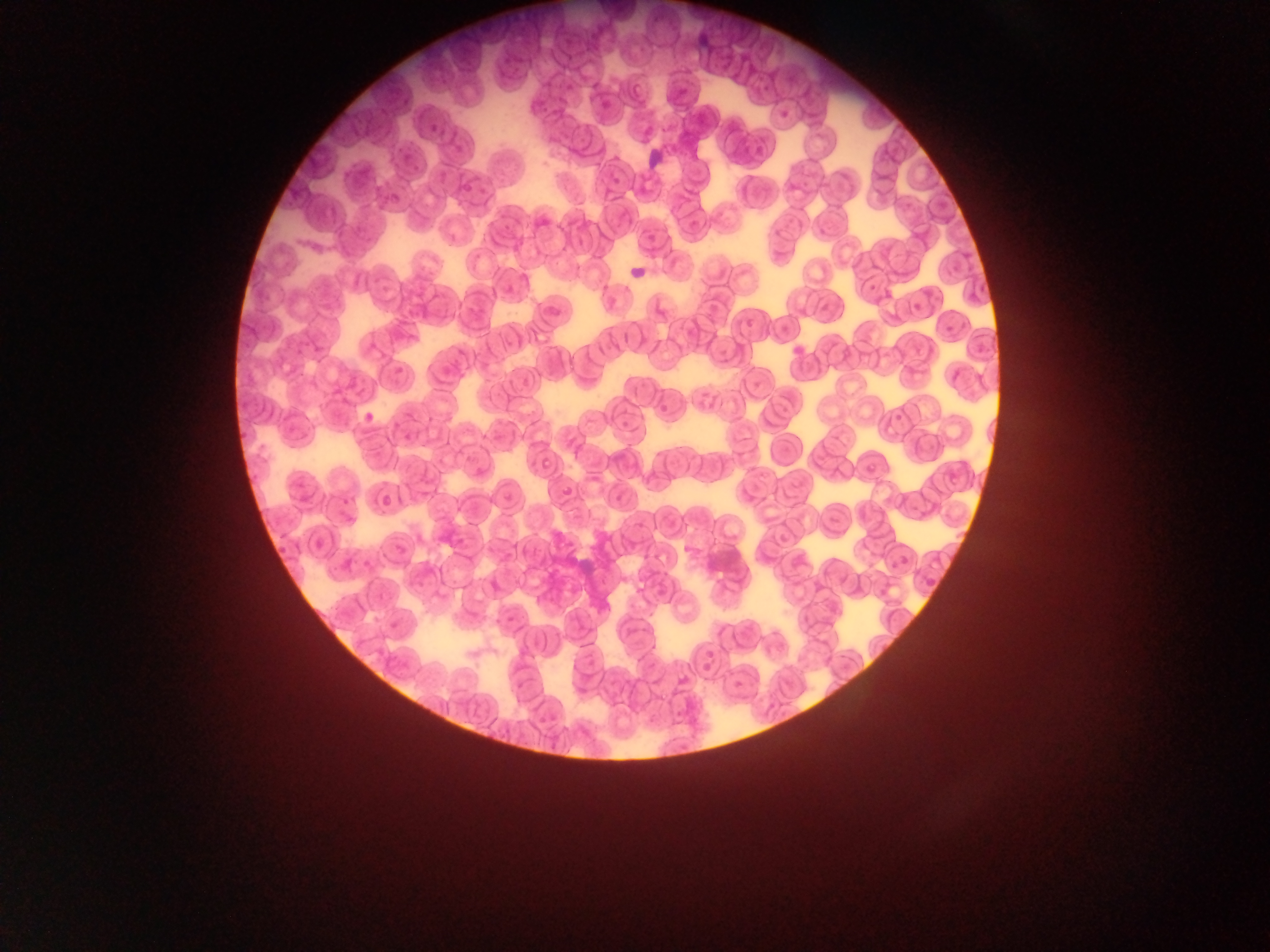
Approximate bounding boxes as {left, top, right, bottom} in pixels. Plasmodium parasite locations: {778, 100, 800, 119}, {425, 120, 443, 133}, {942, 319, 960, 337}, {788, 343, 807, 355}, {393, 364, 409, 382}, {888, 552, 913, 574}. Leukocyte locations: {642, 137, 670, 173}. Single field of view. Mobile-phone photograph taken through the microscope. Image is 1270×952 pixels. Sample from Ghana. Thin blood smear.